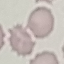
Malaria status: uninfected. Cell patch, automatically extracted from a larger field of view and resized to 64 × 64 pixels. Giemsa stain. Thin smear of blood. Acquired by smartphone through the microscope eyepiece.